Assess this cell for malaria.
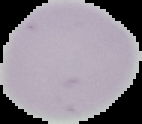
It is uninfected.

Summary:
  - Preparation: thin blood smear
  - Image type: segmented cell region with the area outside set to black
  - Image size: 142×124 pixels